Point out each malaria parasite.
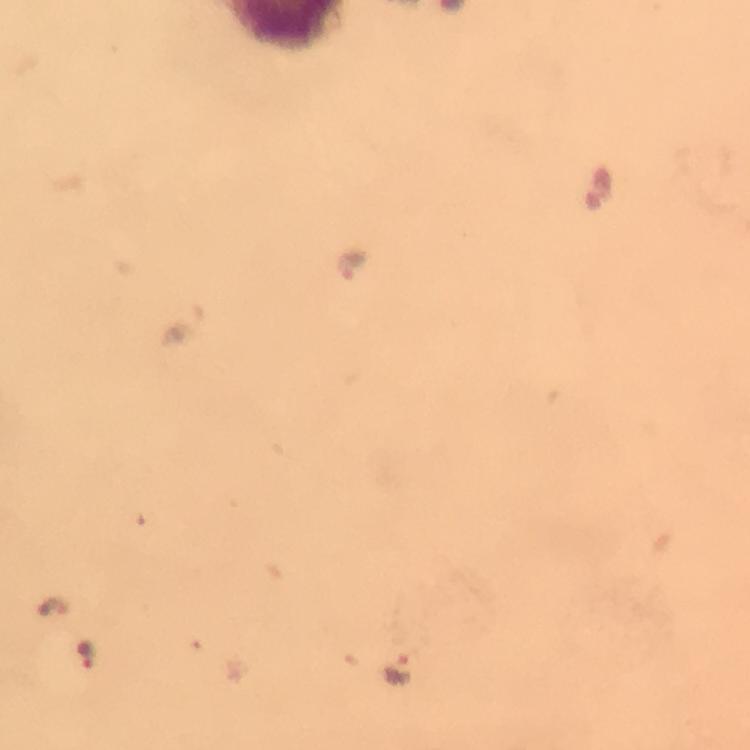
Approximate centers as [x, y] in pixels.
Malaria parasites: [353, 263], [55, 608], [88, 654], [396, 669].

Summary:
  - Preparation: thick blood film
  - Capture: smartphone camera through the microscope
  - Stain: Giemsa
  - Context: from a diagnostic examination for malaria
  - Magnification: 100x
  - Immersion oil: applied
  - Image size: 750×750 pixels
  - Cropped from: one field of view